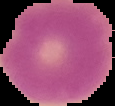

Summary:
  - Image size: 115×106 pixels
  - Preparation: thin blood smear
  - Image type: segmented cell region on a black background
  - Result: no Plasmodium parasites detected